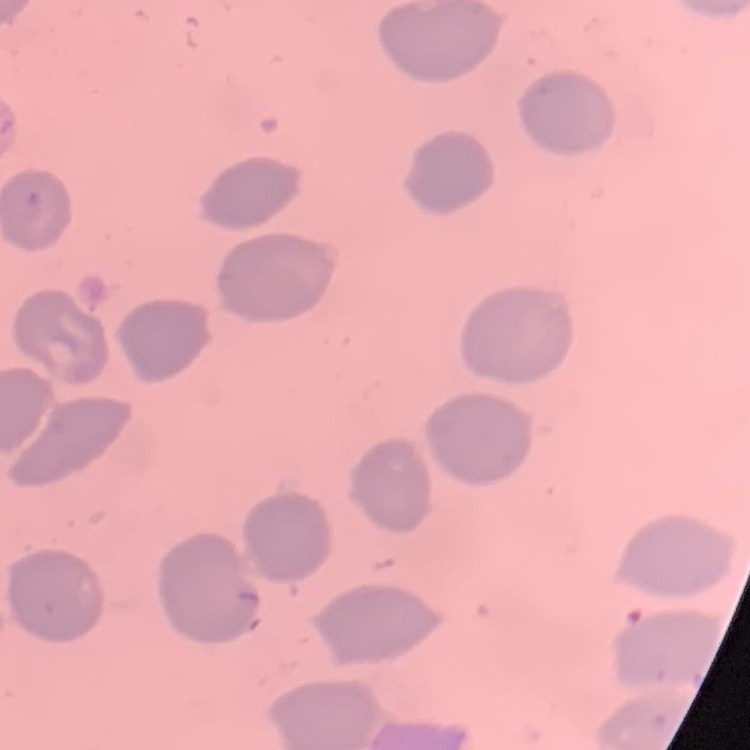 The red blood cells exhibit no rouleaux formation. Square crop of a larger photomicrograph. Thin peripheral smear. Stained with either Field's or Giemsa.